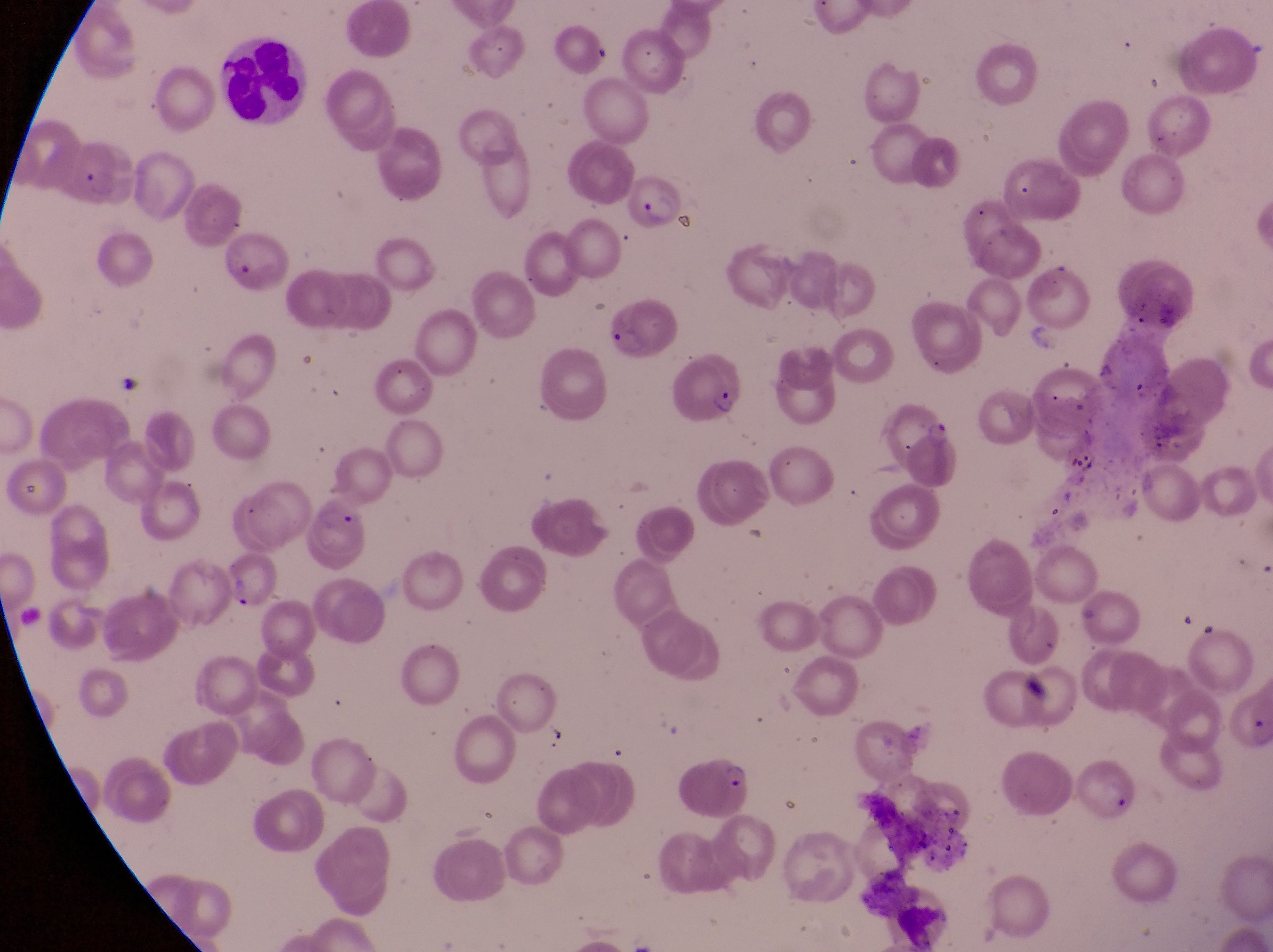

Approximate bounding boxes as (left, top, right, bottom) in pixels.
Summary:
  - Trophozoite locations: (78, 167, 121, 206), (919, 419, 956, 451)
  - Parasitised red blood cell locations: (624, 165, 689, 230), (607, 305, 670, 358), (667, 355, 745, 425), (307, 499, 374, 577), (218, 556, 278, 619), (681, 747, 758, 824)
  - Leukocyte locations: (218, 33, 308, 130)
  - Magnification: 1000x
  - Image size: 1273×952 pixels
  - Country: Uganda
  - Capture: smartphone photograph through the eyepiece of an Olympus CX-23 microscope
  - Preparation: thin blood film
  - Field of view: single